Point out each Plasmodium parasite and each leukocyte.
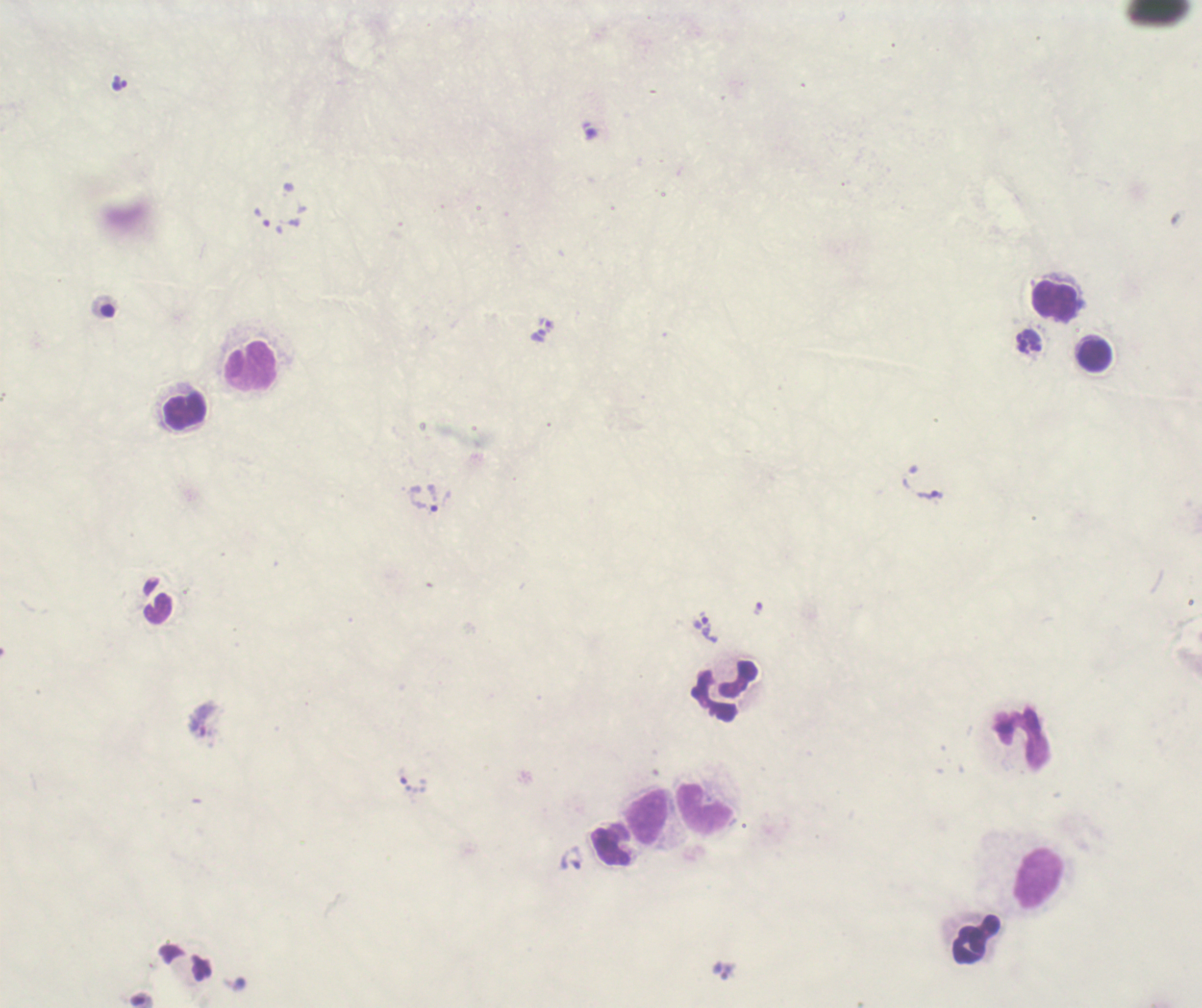
Approximate centers as [x, y] in pixels.
Trophozoites: [119, 83], [929, 494], [423, 498], [757, 608], [706, 627], [203, 719].
No schizont or gametocyte forms observed.
Leukocytes: [1055, 302], [1094, 355], [251, 367], [187, 410], [725, 691], [1021, 739], [705, 809], [649, 818], [1038, 879], [977, 940].

{
  "stain": "Romanowsky",
  "preparation": "thick blood smear",
  "field_of_view": "single",
  "magnification": "100x",
  "context": "previously used in an actual diagnosis",
  "image_size": "1202×1008 pixels",
  "coloration_quality": "bad",
  "background_quality": "unsatisfactory"
}